Classify this cell by malaria status.
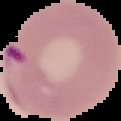
It is parasitized.

Summary:
  - Image size: 121×121 pixels
  - Preparation: thin blood smear
  - Image type: cell region segmented out of the field of view; surrounding area masked to black